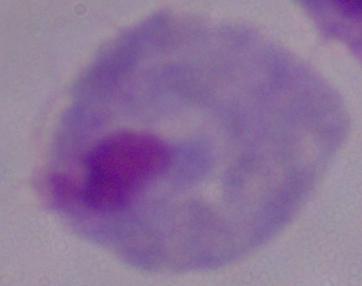
magnification = 1000x
identification = trichomonad
modality = micrograph